Classify this cell by malaria status.
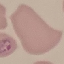
It is parasitized.

{
  "stain": "Giemsa",
  "image_type": "automatically extracted cell patch, resized to 64 × 64 pixels",
  "preparation": "thin blood film",
  "capture": "smartphone camera at the microscope eyepiece"
}